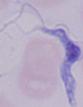
Captured at 1000x magnification. A trypanosome is seen. Micrograph.